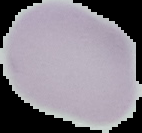

image size = 142×133 pixels
malaria status = uninfected
image type = segmented cell region with the area outside set to black
preparation = thin blood film